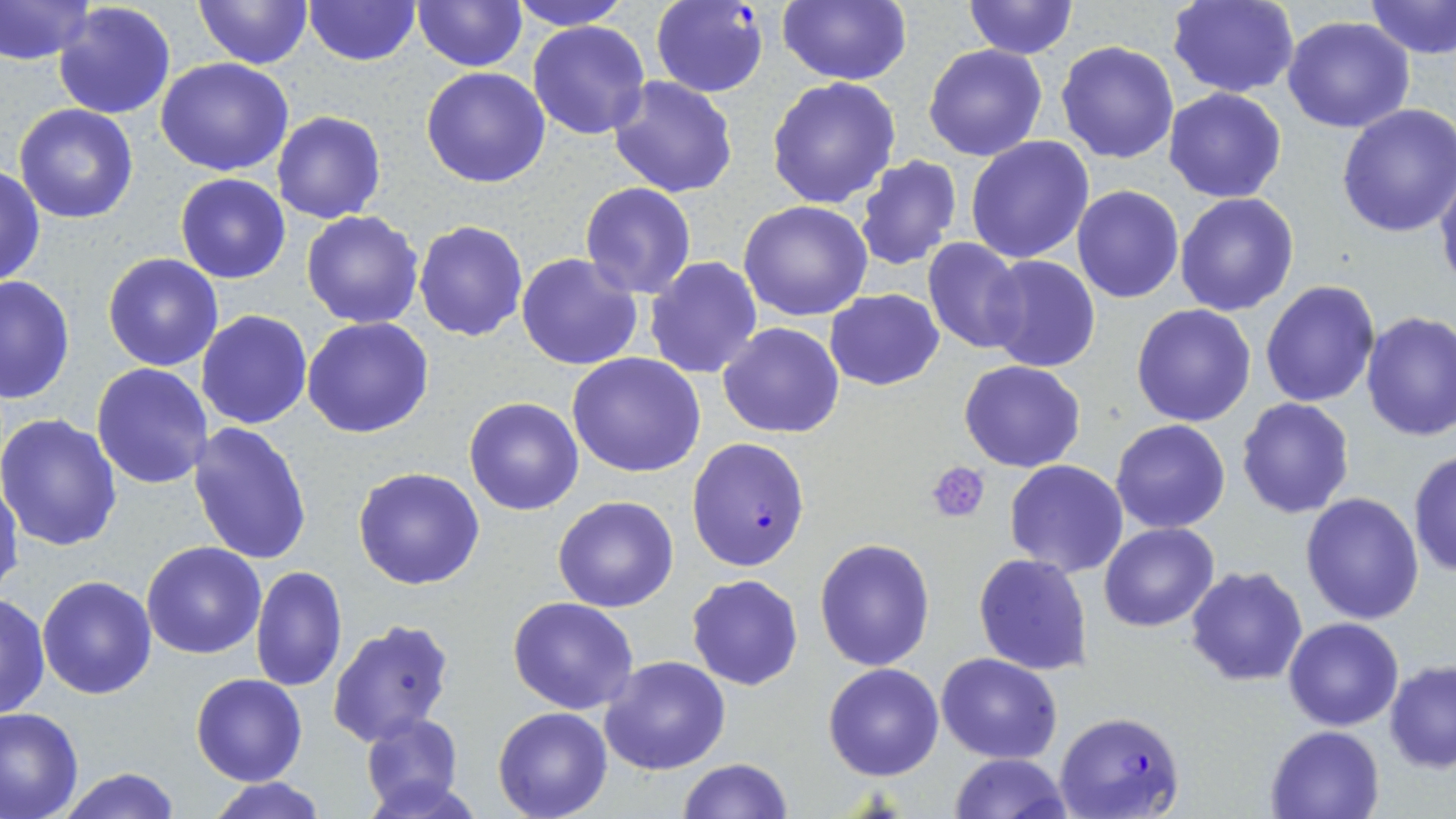

slide-level diagnosis = Plasmodium falciparum
uninfected red blood cell locations = approximate bounding boxes as (x1,y1)-(x2,y2) corner pairs in pixels: (0,0)-(95,65), (193,0)-(311,69), (506,0)-(634,30), (779,0)-(912,86), (964,0)-(1079,59), (1167,0)-(1298,98), (1364,0)-(1455,61), (302,1)-(419,67), (411,1)-(527,71), (52,2)-(178,119), (1283,16)-(1415,133), (529,19)-(653,140), (1056,41)-(1181,164), (923,44)-(1048,162), (156,57)-(296,175), (420,66)-(551,187), (609,75)-(739,199), (766,76)-(902,210), (1163,87)-(1287,203), (1336,102)-(1456,238), (14,104)-(139,223), (273,112)-(386,224), (965,136)-(1095,263), (854,154)-(961,272), (0,165)-(46,289), (1435,165)-(1456,299), (175,173)-(291,284), (579,183)-(698,299), (1072,184)-(1184,304), (1174,193)-(1299,316), (738,200)-(873,321), (301,210)-(425,328), (414,219)-(528,341), (922,239)-(1027,355), (103,253)-(225,371), (515,253)-(644,371), (984,255)-(1099,373), (643,257)-(763,378), (0,273)-(74,404), (1260,280)-(1380,408), (824,289)-(945,391), (1131,303)-(1258,427), (194,309)-(313,430), (1360,313)-(1456,443), (302,317)-(434,440), (718,321)-(846,439), (565,351)-(706,478), (959,359)-(1086,472), (92,363)-(213,488), (464,396)-(583,515), (1235,397)-(1356,518), (0,412)-(123,551), (1110,418)-(1232,533), (186,420)-(312,566), (1407,448)-(1456,579), (1003,460)-(1129,577), (354,465)-(485,590), (0,475)-(23,593), (1299,492)-(1425,625), (552,495)-(679,612), (1099,523)-(1219,632), (814,536)-(936,671), (142,540)-(268,658), (973,554)-(1092,676), (1185,565)-(1309,685), (251,566)-(347,693), (686,573)-(805,691), (36,574)-(158,699), (1,592)-(50,720), (508,596)-(640,715), (1282,618)-(1403,731), (326,619)-(456,749), (936,652)-(1063,763), (599,655)-(731,774), (1383,659)-(1456,772), (823,663)-(944,781), (191,673)-(307,786), (493,705)-(613,819), (0,706)-(83,819), (360,712)-(464,814), (1264,724)-(1385,818), (949,753)-(1070,819), (677,757)-(794,818), (54,766)-(182,819), (207,777)-(328,819)
magnification = 1000x
stain = May-Grünwald-Giemsa
platelet locations = approximate bounding boxes as (x1,y1)-(x2,y2) corner pairs in pixels: (925,462)-(992,523)
preparation = thin blood film
image size = 1456×819 pixels
field of view = one of a larger specimen
Plasmodium falciparum-infected red blood cell locations = approximate bounding boxes as (x1,y1)-(x2,y2) corner pairs in pixels: (650,1)-(769,98), (686,437)-(811,571), (1053,709)-(1186,819)
modality = light microscopy